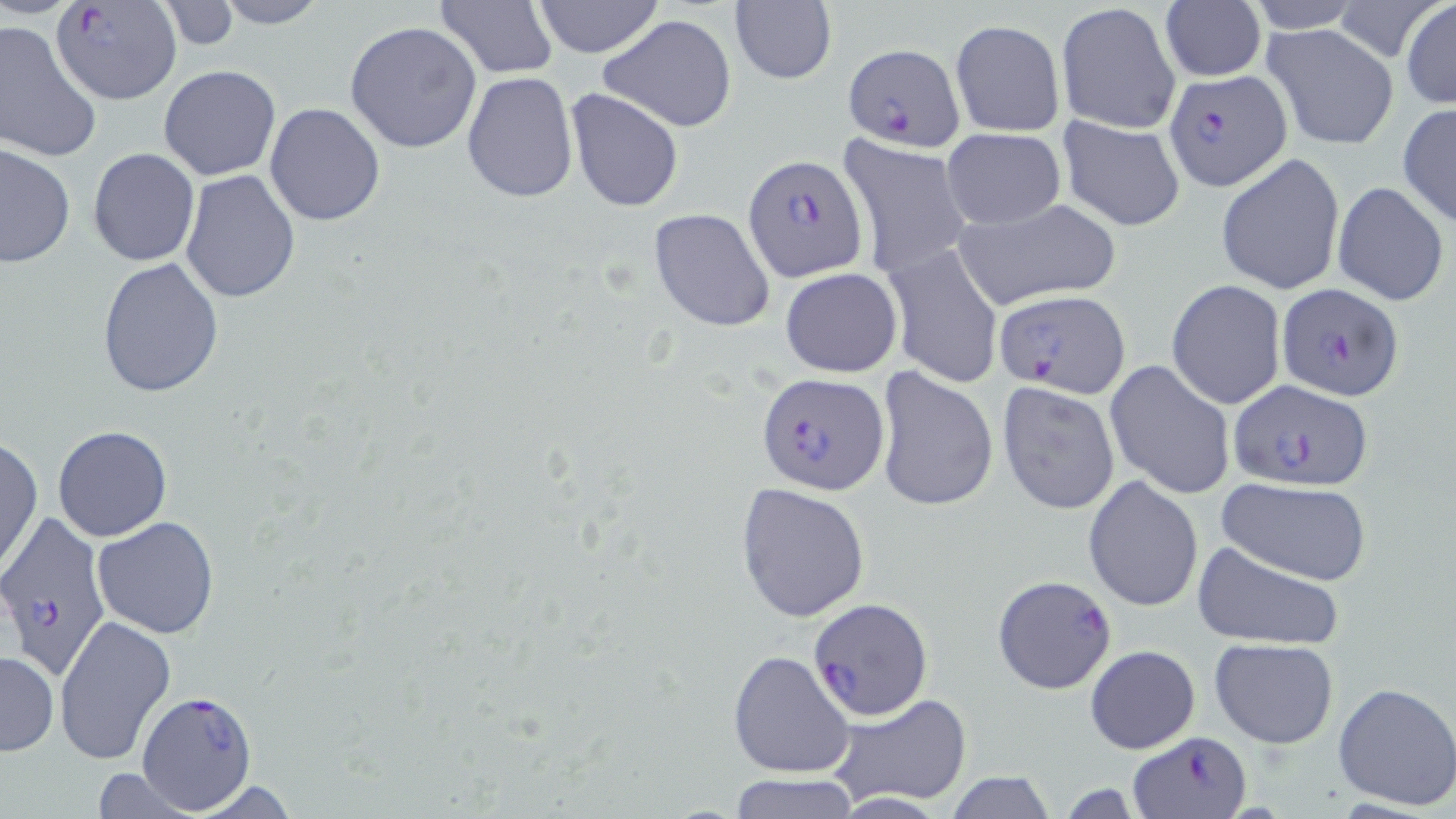
slide-level diagnosis = Plasmodium falciparum
uninfected red blood cell locations = approximate bounding boxes as (x1, y1, x2, y2) in pixels: (212, 0, 333, 28), (530, 0, 666, 58), (1244, 0, 1372, 32), (1159, 1, 1265, 84), (1401, 1, 1456, 108), (434, 2, 560, 78), (726, 2, 838, 86), (1055, 2, 1182, 134), (156, 3, 242, 51), (598, 15, 738, 132), (344, 20, 482, 154), (949, 20, 1065, 136), (0, 21, 101, 163), (1262, 22, 1399, 152), (158, 65, 282, 181), (461, 71, 579, 203), (566, 88, 684, 212), (264, 102, 385, 226), (1397, 103, 1456, 229), (1056, 114, 1187, 234), (941, 128, 1066, 229), (838, 136, 974, 278), (1, 143, 75, 269), (88, 147, 199, 267), (1216, 152, 1346, 296), (179, 169, 302, 304), (1332, 182, 1449, 304), (951, 197, 1122, 310), (648, 207, 777, 332), (883, 241, 1005, 389), (96, 257, 223, 399), (780, 267, 902, 378), (1167, 279, 1286, 408), (1105, 361, 1235, 500), (875, 368, 999, 513), (997, 380, 1121, 516), (53, 424, 172, 541), (0, 436, 42, 576), (1082, 475, 1203, 614), (1216, 478, 1371, 585), (735, 481, 871, 622), (92, 516, 220, 639), (1192, 540, 1345, 651), (992, 575, 1118, 696), (54, 614, 176, 765), (1209, 638, 1339, 749), (1086, 645, 1200, 753), (727, 649, 855, 779), (0, 650, 57, 755), (1332, 680, 1456, 812), (827, 692, 973, 807), (90, 767, 200, 819), (943, 773, 1057, 817), (726, 774, 860, 818), (185, 777, 302, 818)
image size = 1456×819 pixels
modality = optical microscopy
Plasmodium falciparum-infected red blood cell locations = approximate bounding boxes as (x1, y1, x2, y2) in pixels: (53, 2, 183, 105), (840, 43, 966, 150), (1164, 70, 1293, 191), (742, 154, 869, 284), (1276, 283, 1405, 402), (995, 290, 1130, 400), (756, 372, 887, 496), (1226, 379, 1372, 490), (0, 516, 113, 683), (806, 596, 932, 719), (135, 688, 260, 813), (1130, 731, 1252, 817)
stain = May-Grünwald-Giemsa
magnification = 1000x
preparation = thin blood film
field of view = one of a larger specimen